Assess the background quality.
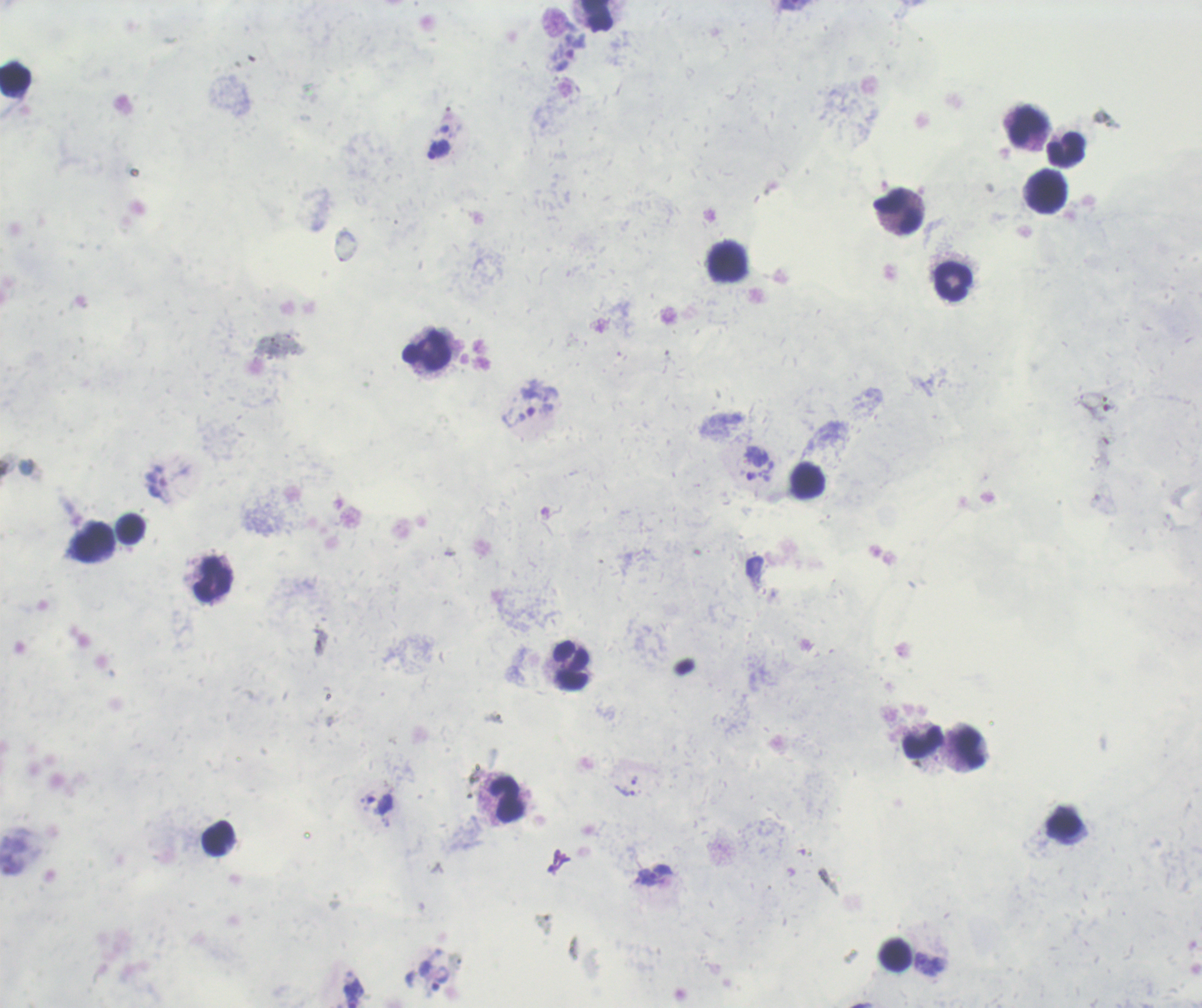
Poor.

Approximate centers as {x, y} in pixels.
Summary:
  - Trophozoite locations: {439, 150}, {634, 780}, {625, 790}, {379, 803}, {648, 876}
  - Leukocyte locations: {597, 15}, {15, 77}, {1030, 125}, {1067, 149}, {1047, 192}, {896, 210}, {728, 261}, {953, 281}, {426, 351}, {808, 481}, {130, 528}, {93, 540}, {213, 579}, {570, 664}, {923, 742}, {970, 748}, {506, 799}, {1065, 826}, {218, 837}, {896, 954}
  - Image size: 1202×1008 pixels
  - Context: previously used in a real diagnosis
  - Preparation: thick smear of blood
  - Stain: Romanowsky
  - Coloration quality: bad
  - Field of view: one from this slide
  - Result: malaria parasites detected
  - Magnification: 100x